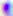
Summary:
  - Magnification: 400x
  - Modality: micrograph
  - Identification: Toxoplasma gondii